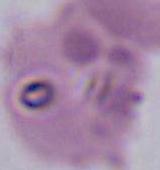
magnification = 400x or 1000x
modality = photomicrograph
identification = Plasmodium